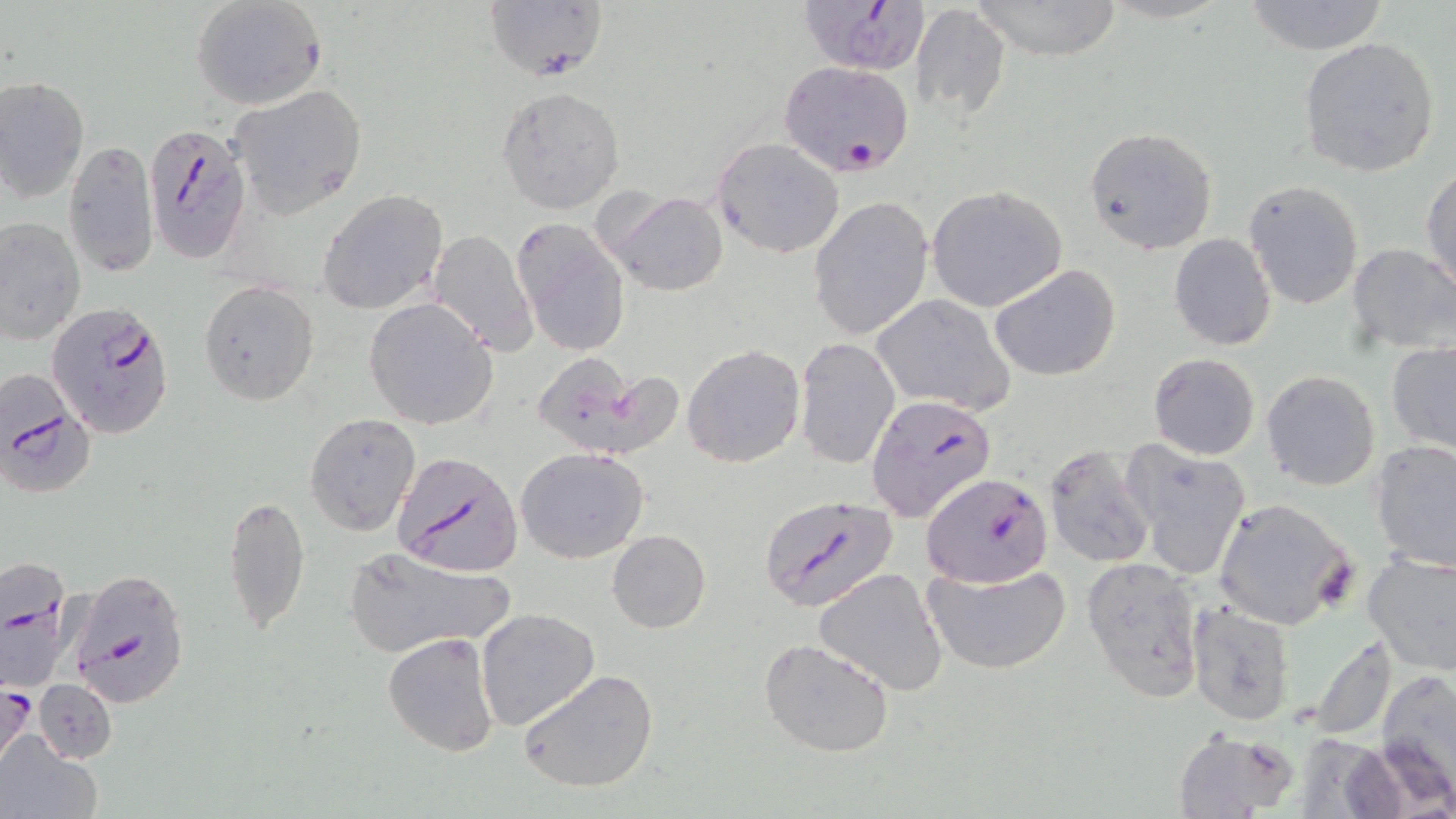 Approximate bounding boxes as (x1,y1)-(x2,y2) corner pairs in pixels. Uninfected red blood cell locations: (485,0)-(611,82), (969,0)-(1124,61), (1241,0)-(1391,54), (191,1)-(327,111), (911,3)-(1012,122), (1299,36)-(1441,179), (1,76)-(88,203), (228,84)-(369,218), (496,86)-(625,214), (1084,126)-(1219,255), (712,136)-(846,258), (63,137)-(159,278), (1422,165)-(1456,296), (1244,179)-(1364,309), (926,185)-(1067,312), (318,189)-(449,315), (603,190)-(728,296), (807,195)-(934,343), (1,216)-(84,344), (511,218)-(630,358), (427,229)-(539,357), (1168,233)-(1278,351), (1346,244)-(1456,355), (990,264)-(1122,382), (199,281)-(319,406), (870,295)-(1017,416), (364,297)-(499,429), (795,337)-(899,469), (1386,340)-(1456,457), (681,343)-(805,467), (538,351)-(682,453), (1148,352)-(1260,459), (1261,371)-(1381,492), (304,411)-(422,538), (1370,439)-(1456,572), (1045,442)-(1157,570), (1120,442)-(1251,580), (516,447)-(650,564), (224,492)-(312,637), (1212,497)-(1358,630), (607,529)-(711,633), (342,547)-(517,657), (1361,550)-(1456,675), (1081,558)-(1207,702), (924,562)-(1072,676), (813,568)-(950,696), (1189,601)-(1295,725), (475,607)-(600,731), (384,632)-(501,758), (1303,632)-(1400,739), (757,637)-(896,758), (1375,667)-(1456,804), (519,669)-(660,794), (35,680)-(116,764), (1172,727)-(1300,818), (1,734)-(103,818). Plasmodium falciparum-infected red blood cell locations: (802,4)-(933,74), (779,60)-(913,177), (144,123)-(250,263), (47,300)-(174,437), (0,372)-(97,489), (866,395)-(997,522), (393,452)-(523,577), (923,472)-(1053,588), (760,492)-(898,614), (0,554)-(75,690), (68,567)-(191,706), (0,682)-(35,768). Slide-level diagnosis: Plasmodium falciparum. Light microscopy. Thin blood smear. May-Grünwald-Giemsa-stained preparation. Image is 1456×819 pixels. Captured at 1000x magnification. Single field of view.